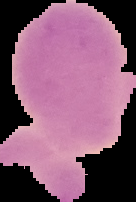
{
  "preparation": "thin blood film",
  "image_type": "segmented cell region on a black background",
  "result": "no Plasmodium parasites seen",
  "image_size": "136×202 pixels"
}